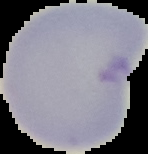

Summary:
  - Malaria status: uninfected
  - Image size: 148×154 pixels
  - Preparation: thin blood film
  - Image type: cell region segmented out of the field of view; surrounding area masked to black